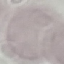
Summary:
  - Result: no malaria parasites detected
  - Image type: cell patch, automatically extracted from a larger field of view and resized to 64 × 64 pixels
  - Preparation: thin blood smear
  - Stain: Giemsa
  - Capture: smartphone camera at the microscope eyepiece